Locate every blood parasite and identify its species.
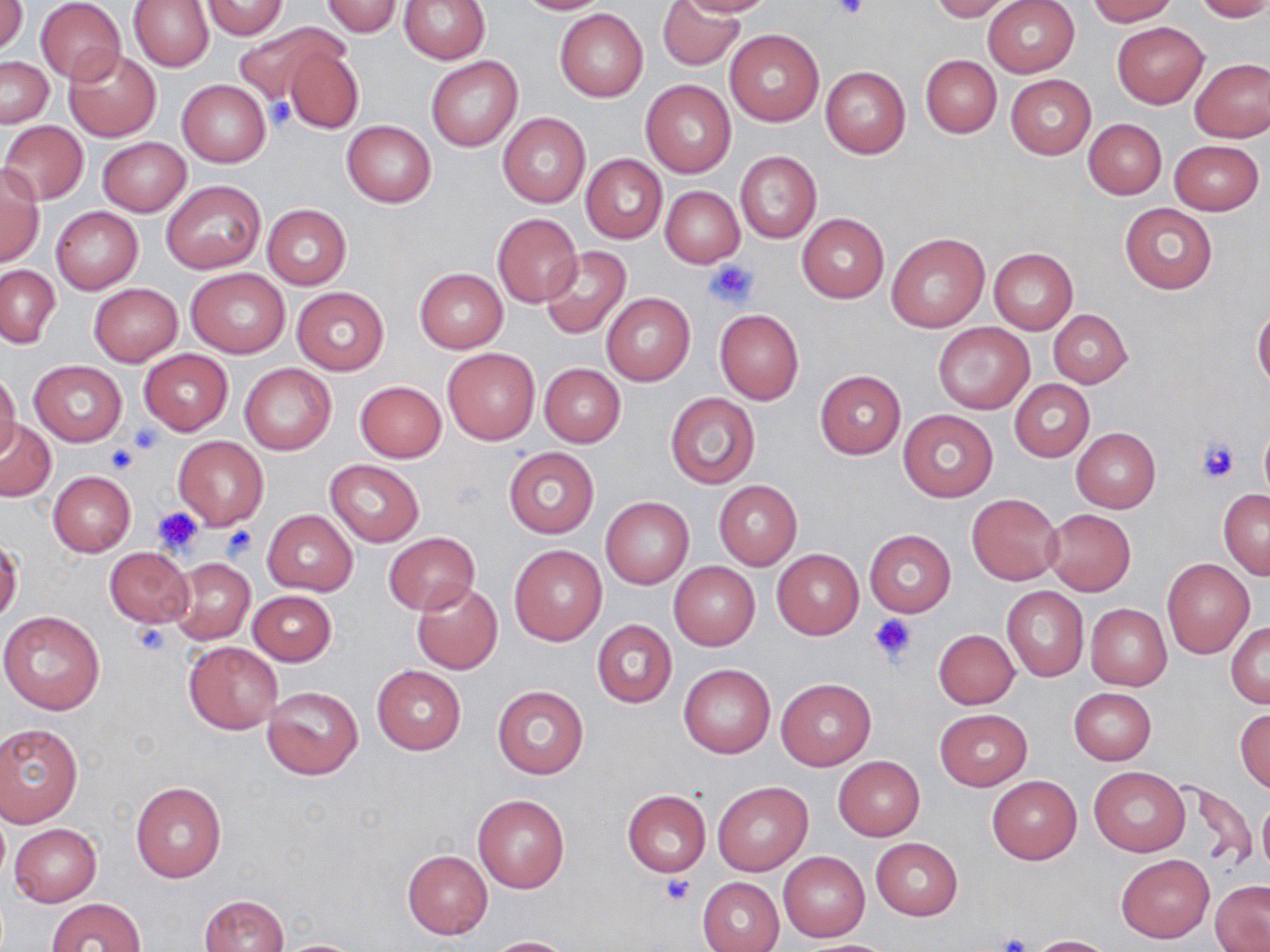
No blood parasites seen.

Summary:
  - Coordinate format: approximate bounding boxes as (x1, y1, x2, y2) in pixels
  - Uninfected red blood cell locations: (1, 0, 27, 54), (398, 0, 490, 62), (515, 0, 610, 15), (657, 0, 743, 71), (673, 0, 776, 17), (928, 0, 1020, 21), (983, 0, 1079, 77), (1087, 0, 1179, 25), (1192, 0, 1270, 22), (35, 1, 126, 84), (128, 1, 213, 71), (201, 1, 289, 39), (321, 1, 404, 37), (554, 8, 648, 101), (230, 22, 341, 107), (1112, 22, 1207, 106), (724, 29, 823, 126), (280, 43, 363, 133), (64, 48, 161, 141), (426, 55, 522, 152), (921, 55, 1001, 137), (1, 57, 53, 127), (1191, 58, 1270, 142), (820, 67, 911, 159), (1005, 75, 1095, 159), (178, 79, 270, 167), (641, 79, 736, 177), (497, 114, 589, 209), (1084, 119, 1166, 198), (2, 120, 88, 204), (341, 120, 436, 207), (97, 137, 191, 216), (1169, 140, 1264, 215), (735, 151, 821, 244), (580, 153, 667, 245), (0, 165, 44, 268), (161, 180, 265, 274), (660, 186, 744, 268), (1120, 202, 1218, 294), (262, 203, 351, 290), (51, 206, 143, 293), (492, 212, 583, 307), (798, 213, 888, 303), (887, 233, 989, 332), (540, 246, 630, 339), (989, 248, 1078, 333), (0, 265, 60, 347), (186, 268, 290, 357), (415, 268, 507, 353), (88, 283, 183, 365), (292, 288, 389, 375), (602, 293, 694, 386), (1253, 308, 1270, 391), (714, 309, 805, 404), (1048, 309, 1132, 387), (932, 322, 1034, 414), (443, 347, 540, 444), (139, 349, 232, 435), (29, 360, 126, 446), (239, 363, 337, 455), (538, 363, 625, 447), (814, 370, 905, 458), (0, 371, 20, 460), (1009, 379, 1093, 462), (354, 380, 446, 462), (664, 393, 760, 488), (898, 409, 999, 502), (1, 419, 57, 502), (1259, 419, 1270, 503), (1071, 427, 1161, 513), (173, 435, 269, 529), (503, 447, 598, 538), (325, 459, 424, 546), (48, 470, 136, 556), (714, 481, 801, 569), (1218, 489, 1270, 579), (968, 494, 1064, 582), (601, 497, 693, 588), (1044, 509, 1136, 596), (262, 510, 358, 596), (865, 529, 956, 616), (383, 533, 479, 613), (509, 545, 606, 646), (103, 547, 194, 628), (772, 550, 862, 639), (169, 559, 255, 645), (1163, 559, 1254, 657), (669, 562, 759, 650), (410, 580, 502, 675), (1001, 587, 1089, 680), (247, 590, 336, 665), (1085, 603, 1172, 691), (0, 610, 106, 714), (591, 619, 678, 707), (1227, 622, 1270, 708), (933, 629, 1019, 708), (183, 641, 282, 733), (371, 663, 466, 754), (679, 663, 775, 758), (776, 679, 875, 770), (261, 685, 364, 780), (492, 685, 588, 779), (1068, 688, 1156, 765), (1235, 708, 1270, 793), (934, 709, 1031, 790), (0, 723, 83, 827), (833, 756, 924, 840), (1089, 767, 1190, 856), (988, 776, 1081, 864), (131, 781, 226, 883), (712, 781, 812, 875), (1173, 781, 1256, 872), (622, 790, 711, 877), (473, 795, 569, 893), (1257, 799, 1270, 878), (9, 823, 102, 906), (871, 837, 962, 920), (402, 849, 492, 939), (780, 852, 870, 941), (1116, 853, 1214, 943), (698, 876, 784, 952), (1210, 880, 1270, 951), (200, 894, 289, 952), (46, 898, 146, 952), (1028, 935, 1117, 952), (485, 936, 578, 952), (270, 938, 369, 951), (798, 939, 899, 951)
  - Platelet locations: (833, 0, 870, 21), (264, 97, 294, 131), (706, 258, 758, 307), (131, 423, 165, 453), (1194, 437, 1241, 483), (105, 442, 136, 474), (153, 506, 204, 556), (221, 524, 258, 562), (869, 614, 918, 666), (131, 621, 172, 656), (662, 874, 695, 906), (996, 933, 1031, 952)
  - Slide-level diagnosis: no evidence of blood parasites
  - Image size: 1270×952 pixels
  - Preparation: thin blood film
  - Modality: optical microscopy
  - Stain: May-Grünwald-Giemsa
  - Field of view: one of a larger specimen
  - Magnification: 1000x